Comment on the morphology of the erythrocytes.
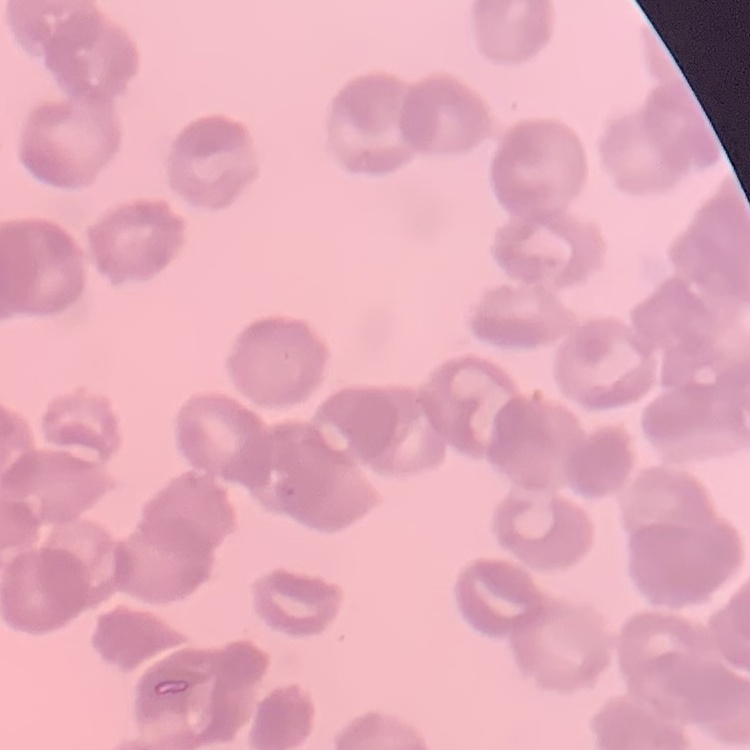

They show rouleaux formation.

Summary:
  - Stain: Field's or Giemsa
  - Image type: square crop of a larger photomicrograph
  - Preparation: thin blood smear